Outline every parasitised red blood cell.
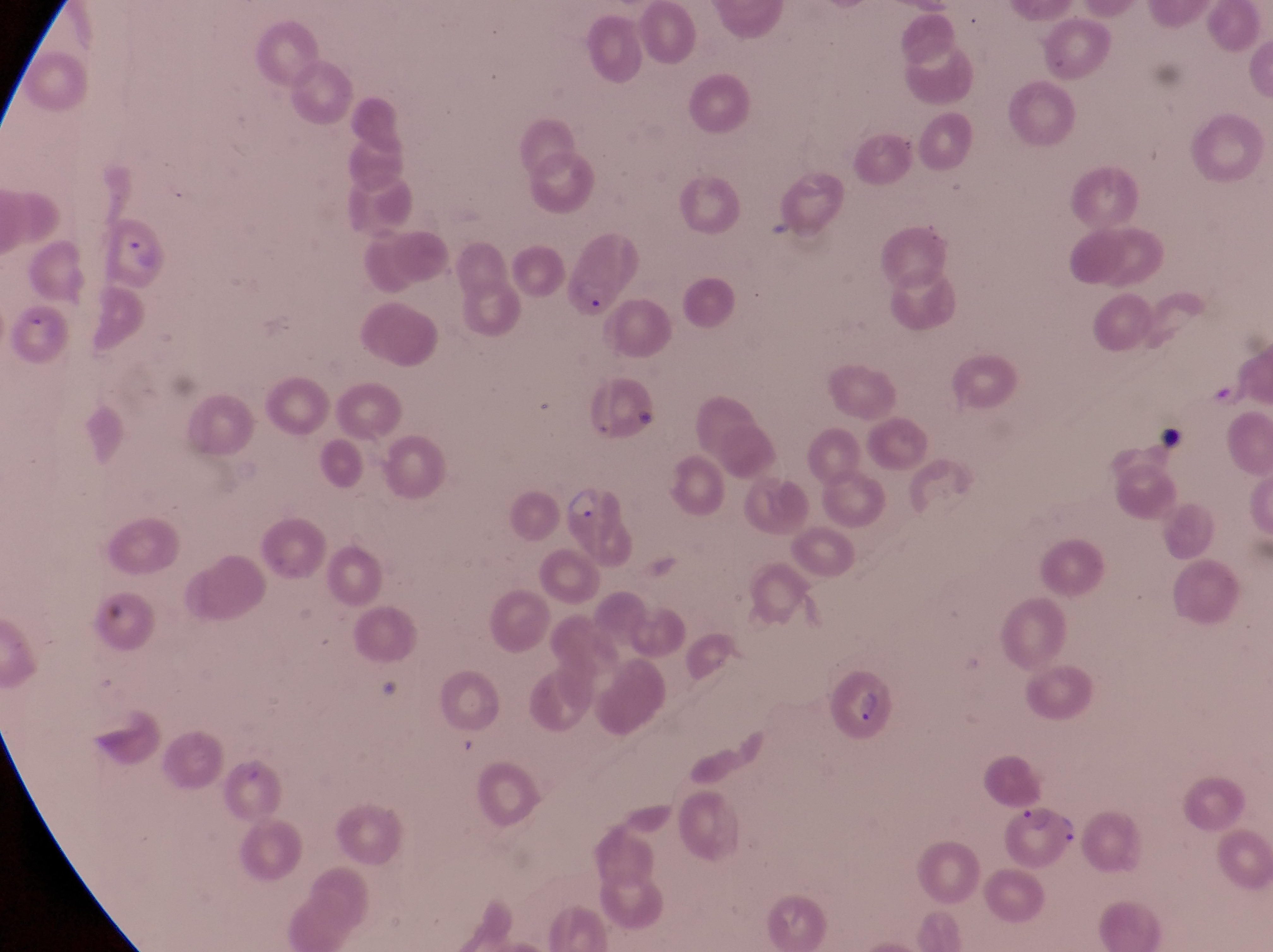

Approximate bounding boxes as [left, top, right, bottom] in pixels.
Parasitised red blood cells: [100, 218, 169, 283], [556, 227, 641, 315], [824, 665, 894, 735], [1006, 796, 1083, 866].

Summary:
  - Trophozoite locations: [565, 484, 602, 524]
  - Artifact (platelet-like body, stain precipitate, or debris) locations: [761, 212, 793, 249], [1153, 424, 1183, 459]
  - Magnification: 1000x
  - Country: Uganda
  - Image size: 1273×952 pixels
  - Capture: smartphone photograph through the eyepiece of an Olympus CX-23 microscope
  - Field of view: single
  - Preparation: thin blood film